Locate every Plasmodium vivax-infected red blood cell.
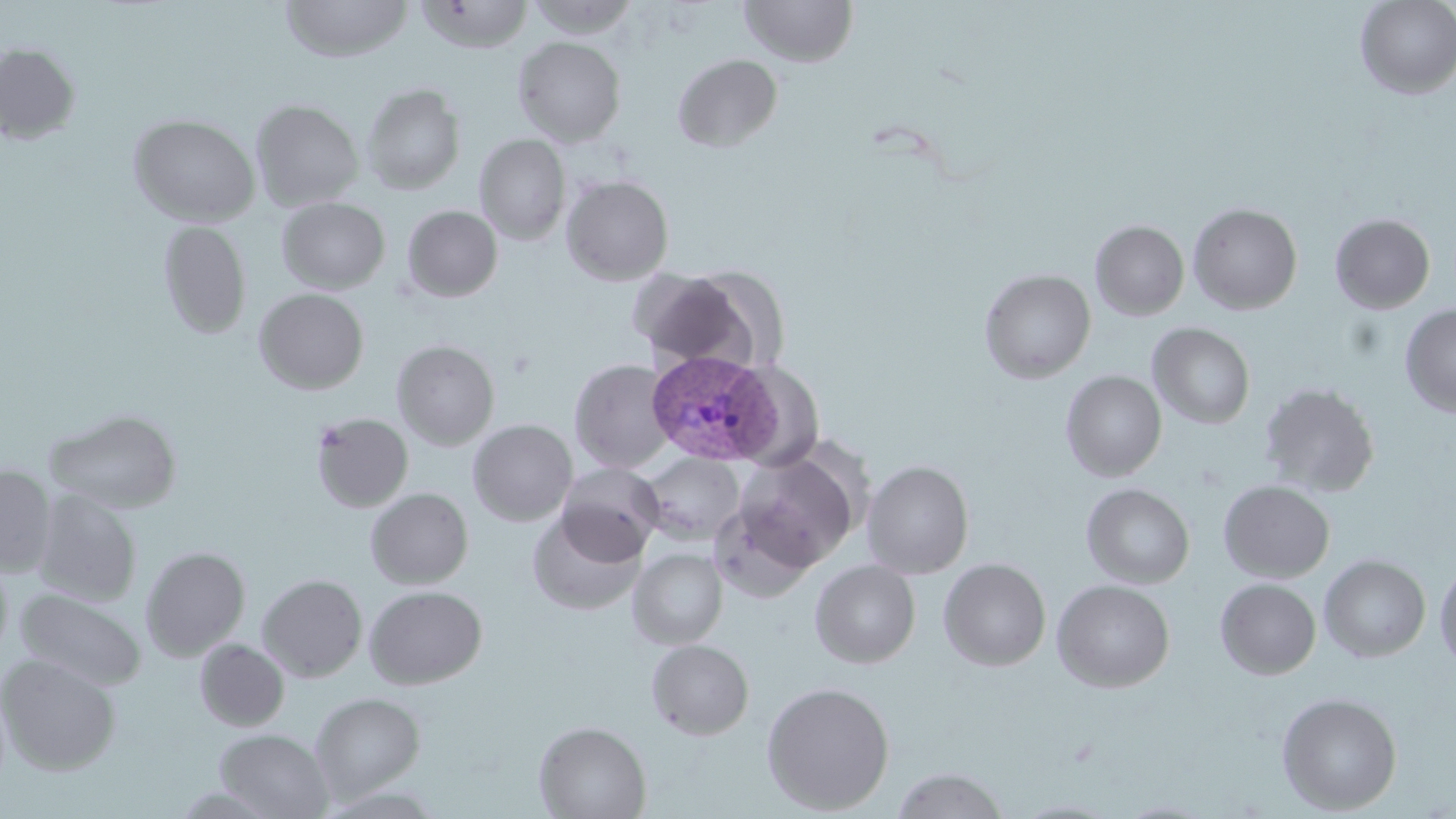

Approximate bounding boxes as named x1/y1/x2/y2 corners in pixels.
Plasmodium vivax-infected red blood cells: (x1=645, y1=348, x2=783, y2=464).

slide-level diagnosis = Plasmodium vivax
field of view = one of a larger specimen
image size = 1456×819 pixels
preparation = thin blood film
magnification = 1000x
uninfected red blood cell locations = approximate bounding boxes as named x1/y1/x2/y2 corners in pixels: (x1=280, y1=0, x2=413, y2=62), (x1=416, y1=0, x2=535, y2=53), (x1=525, y1=0, x2=641, y2=39), (x1=740, y1=0, x2=858, y2=67), (x1=1355, y1=0, x2=1456, y2=99), (x1=513, y1=36, x2=626, y2=146), (x1=0, y1=42, x2=81, y2=145), (x1=672, y1=53, x2=783, y2=152), (x1=362, y1=83, x2=466, y2=194), (x1=250, y1=99, x2=364, y2=211), (x1=129, y1=114, x2=260, y2=227), (x1=475, y1=134, x2=571, y2=244), (x1=561, y1=175, x2=674, y2=285), (x1=277, y1=198, x2=390, y2=294), (x1=1187, y1=203, x2=1303, y2=315), (x1=402, y1=205, x2=502, y2=302), (x1=1330, y1=213, x2=1435, y2=314), (x1=158, y1=220, x2=251, y2=339), (x1=1090, y1=220, x2=1189, y2=320), (x1=630, y1=268, x2=754, y2=370), (x1=979, y1=268, x2=1096, y2=383), (x1=254, y1=288, x2=370, y2=394), (x1=1399, y1=304, x2=1456, y2=417), (x1=1148, y1=323, x2=1255, y2=429), (x1=392, y1=340, x2=500, y2=450), (x1=569, y1=358, x2=676, y2=474), (x1=1061, y1=370, x2=1166, y2=481), (x1=1259, y1=382, x2=1381, y2=497), (x1=45, y1=408, x2=182, y2=513), (x1=310, y1=412, x2=414, y2=512), (x1=467, y1=419, x2=577, y2=526), (x1=734, y1=451, x2=860, y2=570), (x1=640, y1=453, x2=744, y2=544), (x1=861, y1=460, x2=974, y2=579), (x1=556, y1=462, x2=663, y2=562), (x1=0, y1=464, x2=56, y2=576), (x1=1219, y1=480, x2=1335, y2=582), (x1=1081, y1=483, x2=1195, y2=588), (x1=365, y1=488, x2=473, y2=589), (x1=33, y1=489, x2=142, y2=607), (x1=709, y1=499, x2=820, y2=601), (x1=527, y1=509, x2=647, y2=616), (x1=141, y1=546, x2=250, y2=660), (x1=628, y1=548, x2=728, y2=649), (x1=0, y1=554, x2=13, y2=665), (x1=1319, y1=555, x2=1431, y2=662), (x1=939, y1=558, x2=1051, y2=671), (x1=810, y1=559, x2=921, y2=669), (x1=1435, y1=561, x2=1456, y2=672), (x1=257, y1=574, x2=367, y2=682), (x1=1215, y1=578, x2=1321, y2=680), (x1=1052, y1=579, x2=1175, y2=693), (x1=364, y1=585, x2=487, y2=689), (x1=16, y1=588, x2=146, y2=691), (x1=194, y1=638, x2=289, y2=731), (x1=646, y1=639, x2=754, y2=740), (x1=0, y1=654, x2=121, y2=774), (x1=761, y1=681, x2=895, y2=815), (x1=310, y1=692, x2=425, y2=802), (x1=1277, y1=692, x2=1402, y2=815), (x1=534, y1=721, x2=651, y2=819), (x1=215, y1=729, x2=334, y2=819), (x1=891, y1=767, x2=1010, y2=818)
stain = May-Grünwald-Giemsa
modality = optical microscopy